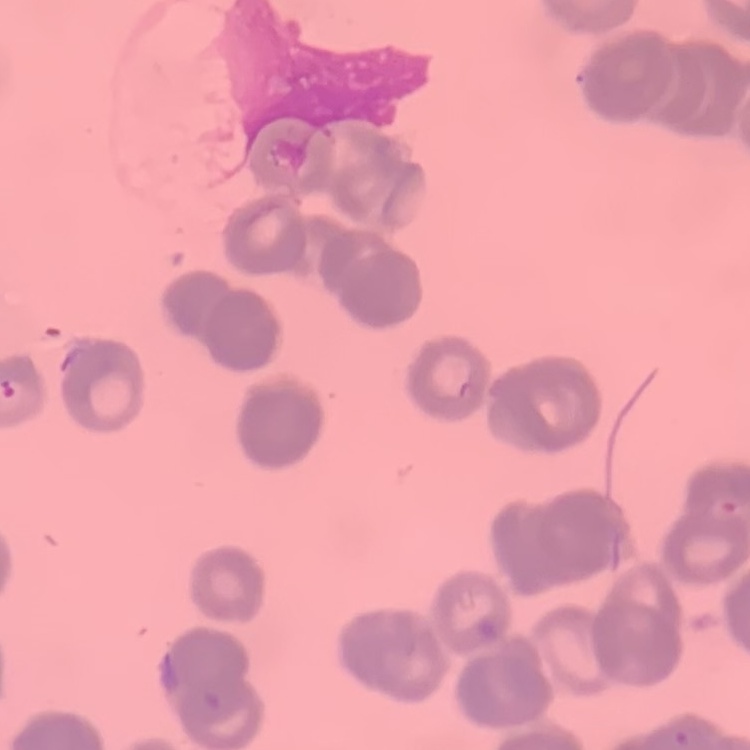
Summary:
  - Erythrocyte morphology: rouleaux formation
  - Image type: square crop of a larger photomicrograph
  - Preparation: thin peripheral smear
  - Stain: Field's or Giemsa